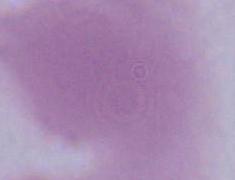

magnification = 1000x
identification = erythrocyte
modality = photomicrograph